Assess for Plasmodium parasites.
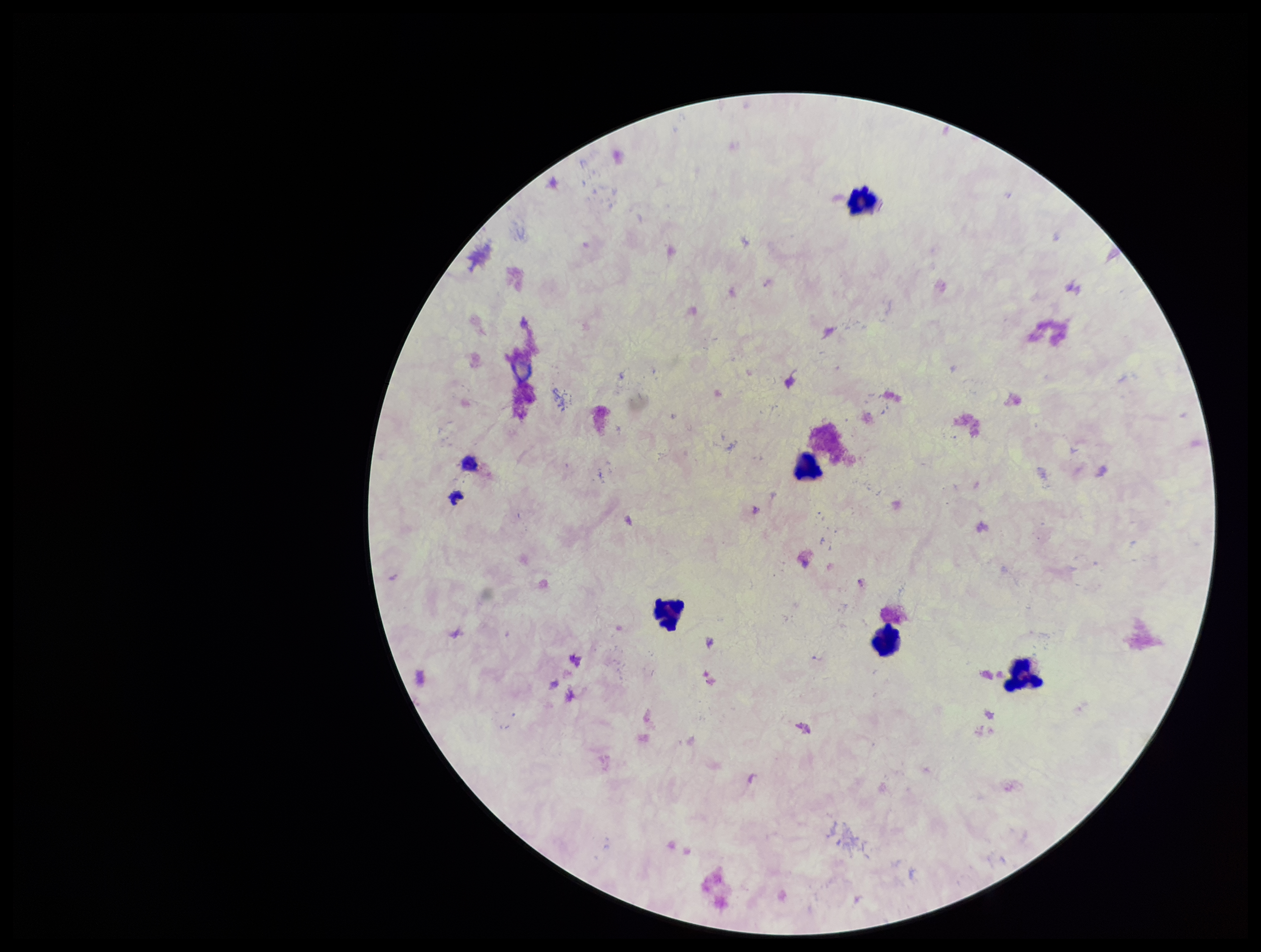
None identified.

Photographed through the microscope eyepiece with a smartphone camera. Leukocyte count: 5. Giemsa stain. Parasite count: 0. Patient malaria status: negative. Image is 1261×952 pixels. One field from this slide. Preparation: thick blood smear.